Report the malaria status of this cell.
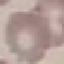
Uninfected.

Summary:
  - Image type: automatically extracted cell patch, resized to 64 × 64 pixels
  - Preparation: thin smear
  - Stain: Giemsa
  - Capture: smartphone camera at the microscope eyepiece